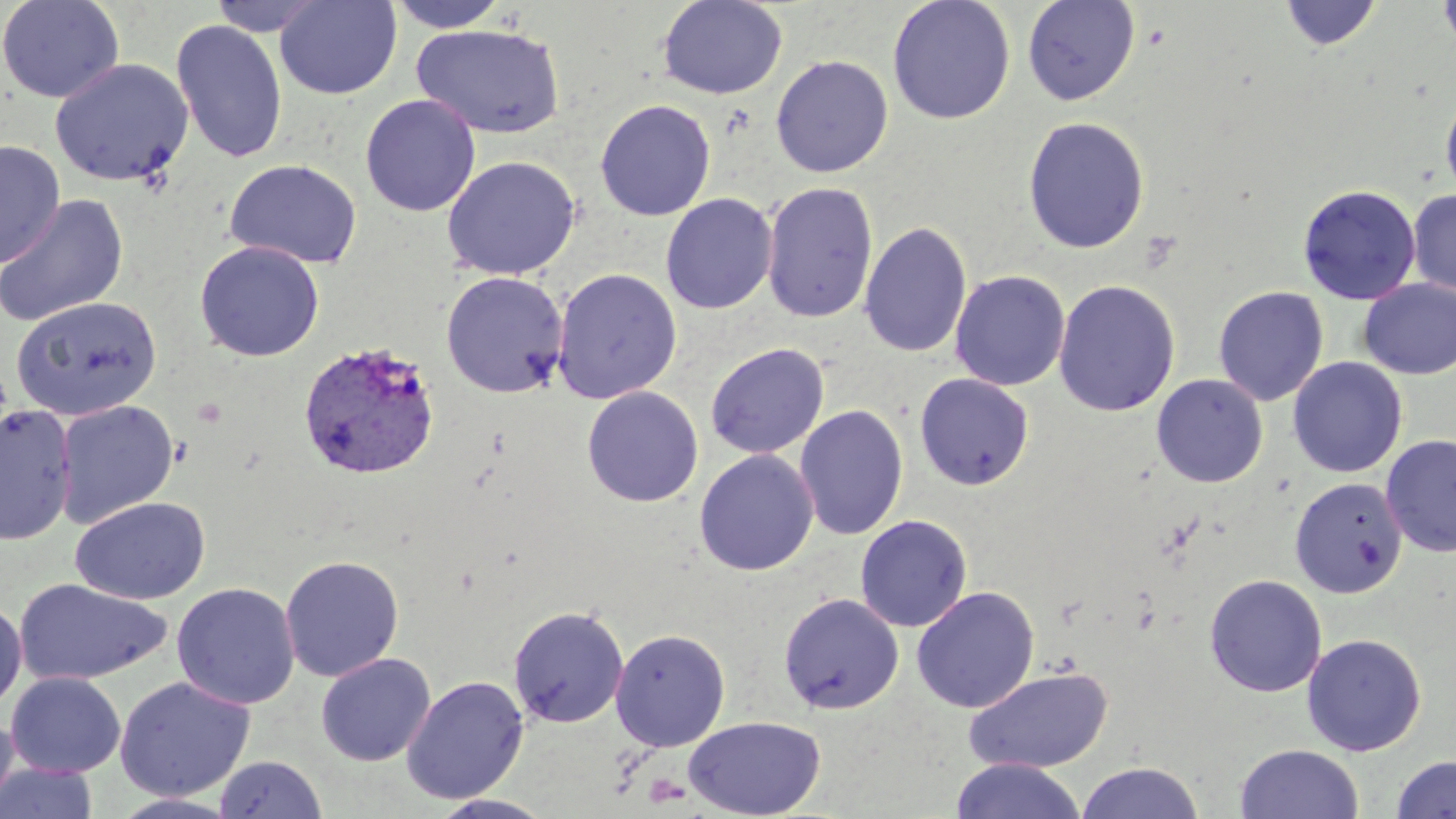
Summary:
  - Coordinate format: approximate bounding boxes as (x1,y1)-(x2,y2) corner pairs in pixels
  - Uninfected red blood cell locations: (0,0)-(125,104), (208,0)-(329,37), (275,0)-(402,99), (385,0)-(513,33), (1438,0)-(1456,53), (657,1)-(788,99), (887,1)-(1015,124), (1022,1)-(1141,105), (1280,1)-(1383,50), (171,19)-(288,163), (412,23)-(566,139), (771,55)-(893,177), (50,57)-(194,187), (1440,84)-(1456,208), (360,94)-(481,216), (595,99)-(716,221), (1022,116)-(1150,254), (0,140)-(65,269), (441,155)-(580,280), (225,158)-(361,268), (762,181)-(878,324), (1298,184)-(1421,305), (1407,189)-(1456,297), (661,193)-(778,315), (1,195)-(129,326), (859,221)-(972,359), (194,240)-(324,361), (552,267)-(682,403), (440,270)-(569,398), (950,270)-(1070,391), (1358,278)-(1456,379), (1053,279)-(1181,417), (1213,286)-(1328,406), (11,296)-(162,421), (705,342)-(829,459), (1287,357)-(1407,478), (914,372)-(1034,491), (1151,373)-(1268,488), (581,386)-(704,507), (54,399)-(179,527), (794,404)-(908,541), (0,405)-(77,545), (1381,434)-(1456,558), (694,449)-(818,576), (1290,478)-(1407,598), (71,496)-(211,605), (855,515)-(972,632), (280,554)-(404,681), (1204,574)-(1327,697), (14,578)-(173,686), (171,582)-(300,710), (911,586)-(1040,713), (778,592)-(904,714), (0,597)-(27,714), (507,605)-(629,728), (610,628)-(730,751), (1301,632)-(1427,756), (316,652)-(435,766), (962,666)-(1114,773), (6,671)-(126,777), (401,675)-(529,804), (114,676)-(255,802), (0,711)-(19,815), (684,715)-(826,818), (1235,744)-(1364,819), (213,755)-(327,818), (1390,755)-(1456,818), (949,758)-(1086,819), (1076,761)-(1204,819), (1,762)-(99,819), (110,792)-(243,818), (429,793)-(556,819)
  - Plasmodium vivax-infected red blood cell locations: (298,341)-(440,480)
  - Slide-level diagnosis: Plasmodium vivax
  - Preparation: thin blood film
  - Modality: optical microscopy
  - Field of view: single
  - Magnification: 1000x
  - Image size: 1456×819 pixels
  - Stain: May-Grünwald-Giemsa